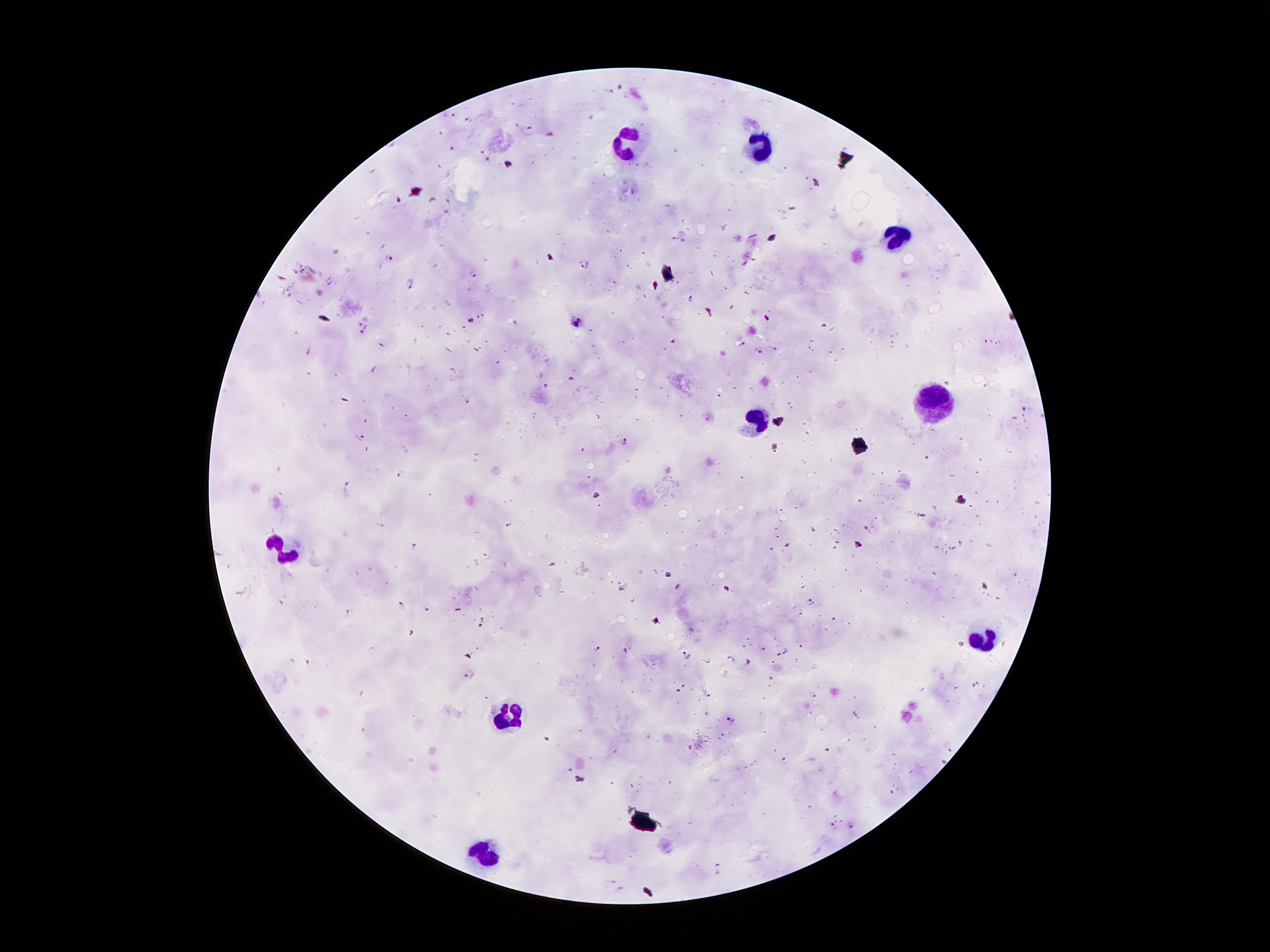

Approximate centers as {x, y} in pixels.
Summary:
  - Plasmodium parasite locations: {452, 115}, {469, 119}, {530, 130}, {451, 150}, {481, 151}, {489, 160}, {675, 237}, {684, 241}, {389, 257}, {585, 265}, {474, 276}, {410, 283}, {691, 299}, {578, 322}, {364, 333}, {672, 342}, {996, 342}, {742, 344}, {775, 347}, {758, 350}, {309, 352}, {374, 370}, {469, 402}, {1024, 409}, {360, 435}, {624, 441}, {582, 451}, {401, 476}, {348, 488}, {509, 524}, {859, 544}, {414, 546}, {811, 602}, {402, 604}, {429, 606}, {349, 611}, {598, 647}, {761, 649}, {787, 651}, {687, 655}, {778, 655}, {732, 659}, {471, 675}, {705, 691}, {813, 694}, {732, 720}, {784, 760}, {569, 771}, {834, 826}, {851, 826}, {719, 869}, {611, 881}, {622, 890}
  - Leukocyte locations: {634, 149}, {760, 152}, {890, 242}, {938, 400}, {757, 422}, {289, 552}, {986, 639}, {508, 709}, {489, 856}
  - Preparation: thick blood smear
  - Stain: Giemsa
  - Image size: 1270×952 pixels
  - Field of view: one from this slide
  - Capture: smartphone camera through the microscope eyepiece
  - Patient malaria status: infected with Plasmodium falciparum
  - Magnification: 100x